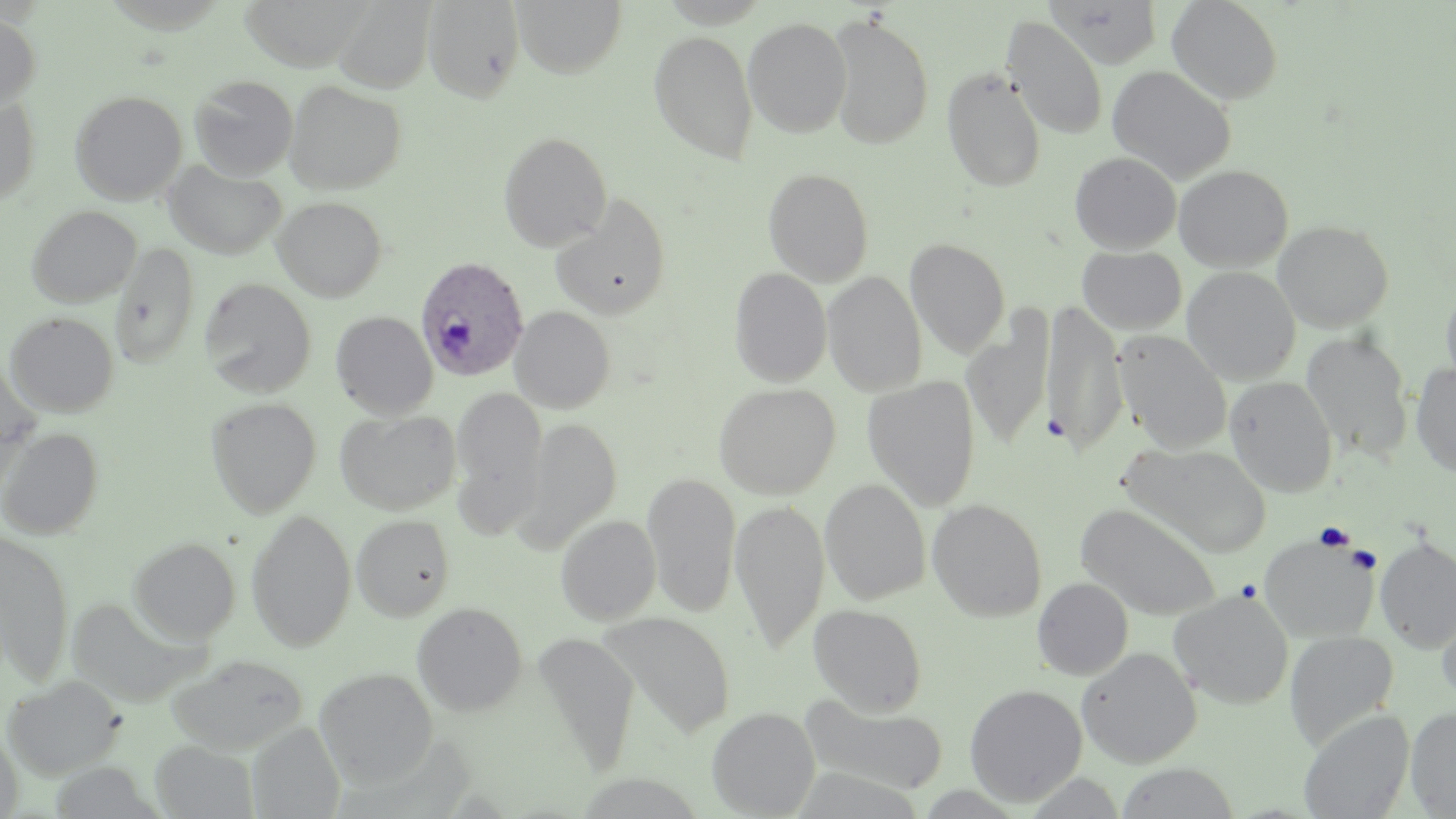
Summary:
  - Coordinate format: approximate bounding boxes as (x1,y1)-(x2,y2) corner pairs in pixels
  - Uninfected red blood cell locations: (240,0)-(371,70), (422,0)-(525,103), (512,0)-(626,77), (1166,0)-(1284,105), (335,1)-(435,93), (1045,1)-(1167,69), (0,12)-(41,111), (826,14)-(935,150), (743,17)-(852,137), (1002,17)-(1108,140), (648,29)-(759,165), (1107,65)-(1237,183), (942,68)-(1046,192), (189,75)-(298,179), (284,80)-(406,195), (70,90)-(188,204), (0,96)-(40,205), (498,131)-(613,251), (1070,152)-(1181,253), (164,160)-(287,259), (1173,164)-(1293,271), (763,167)-(874,286), (550,193)-(673,319), (272,196)-(387,302), (27,205)-(141,307), (1272,219)-(1394,332), (905,237)-(1010,358), (109,243)-(200,369), (1077,246)-(1187,334), (1075,253)-(1277,353), (1181,266)-(1301,385), (729,268)-(832,386), (822,270)-(927,395), (199,278)-(317,397), (1440,282)-(1456,396), (1041,302)-(1128,453), (509,306)-(616,413), (331,310)-(438,419), (4,311)-(119,417), (962,316)-(1054,446), (1113,330)-(1232,453), (1301,330)-(1413,462), (0,360)-(41,496), (1411,363)-(1456,476), (862,376)-(981,511), (1225,376)-(1338,496), (713,383)-(840,499), (450,385)-(547,537), (206,397)-(322,517), (334,409)-(461,515), (518,416)-(622,550), (0,427)-(104,540), (1119,442)-(1271,558), (643,473)-(740,618), (820,479)-(931,604), (927,498)-(1048,622), (730,499)-(829,653), (1075,502)-(1222,620), (246,508)-(356,651), (351,513)-(456,621), (556,514)-(661,625), (0,531)-(74,686), (1258,533)-(1381,643), (128,536)-(240,643), (1375,536)-(1456,652), (1033,577)-(1133,680), (1168,590)-(1294,709), (66,596)-(201,706), (411,601)-(528,716), (1437,601)-(1456,710), (808,604)-(927,716), (602,613)-(736,739), (1284,631)-(1399,750), (531,632)-(639,776), (1077,647)-(1202,768), (166,654)-(308,754), (314,668)-(437,787), (2,675)-(125,779), (964,683)-(1087,806), (799,696)-(950,796), (706,706)-(820,818), (1406,707)-(1456,818), (1299,709)-(1415,819), (248,722)-(345,818), (0,726)-(23,818), (150,740)-(258,818)
  - Plasmodium ovale-infected red blood cell locations: (416,255)-(528,381)
  - Platelet locations: (1043,412)-(1071,442), (1315,522)-(1355,551), (1347,545)-(1380,573), (1235,578)-(1262,602)
  - Slide-level diagnosis: Plasmodium ovale
  - Stain: May-Grünwald-Giemsa
  - Preparation: thin blood film
  - Magnification: 1000x
  - Modality: light microscopy
  - Image size: 1456×819 pixels
  - Field of view: one of a larger specimen